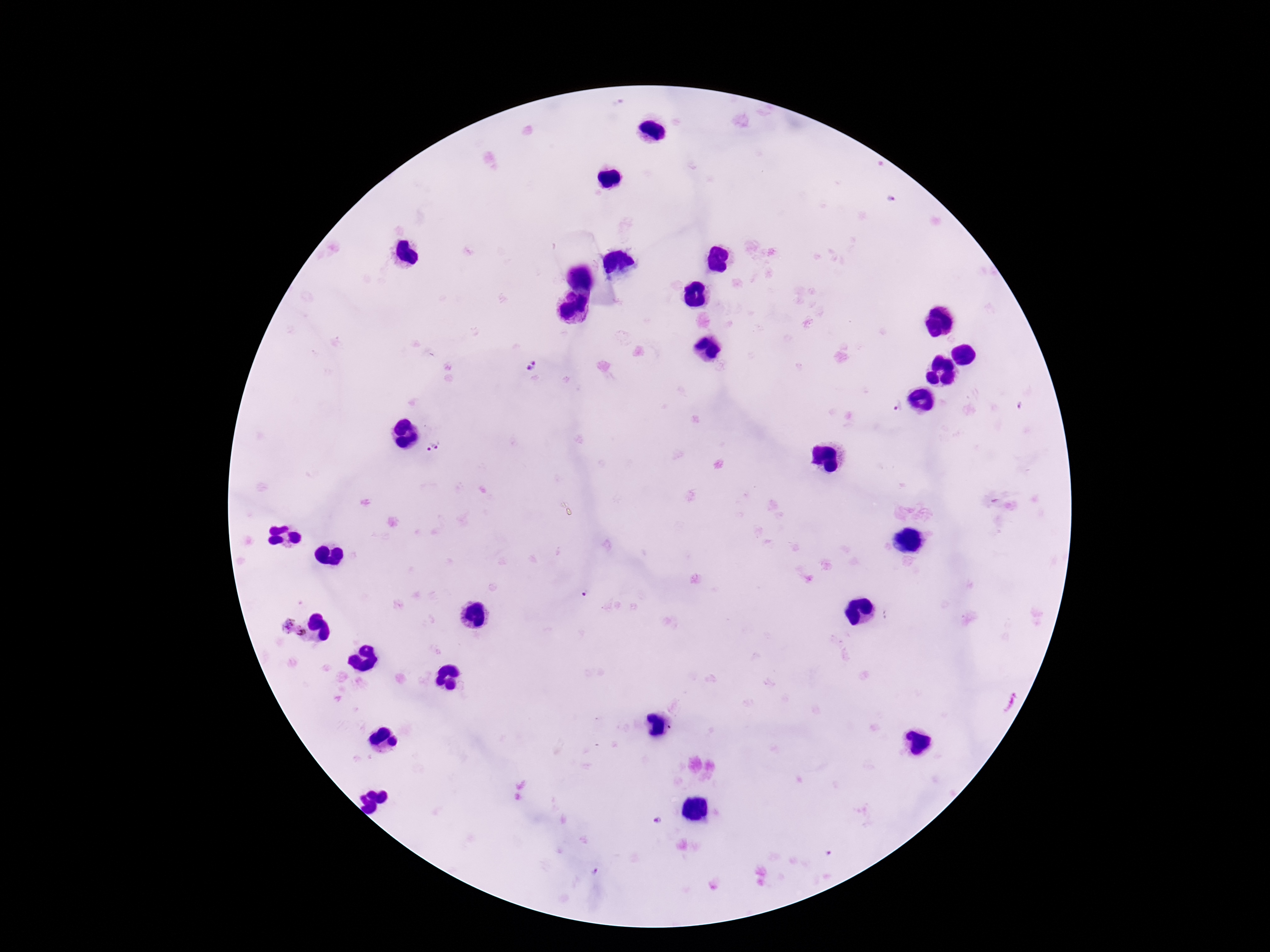
magnification = 100x
Plasmodium parasite locations = approximate centers as {x, y} in pixels: {534, 365}, {899, 406}, {433, 447}, {293, 628}
image size = 1270×952 pixels
patient malaria status = positive
preparation = thick peripheral-blood smear
stain = Giemsa
field of view = single
capture = smartphone camera through the microscope eyepiece